Assess this cell for malaria.
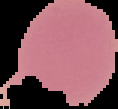
It is uninfected.

From a thin blood film. Image is 118×109 pixels. Cell region segmented out of the field of view; the surrounding area is masked to black.